Report the malaria status of this cell.
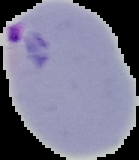

Parasitized.

Summary:
  - Image type: cell region segmented out of the field of view; surrounding area masked to black
  - Image size: 139×160 pixels
  - Preparation: thin blood film